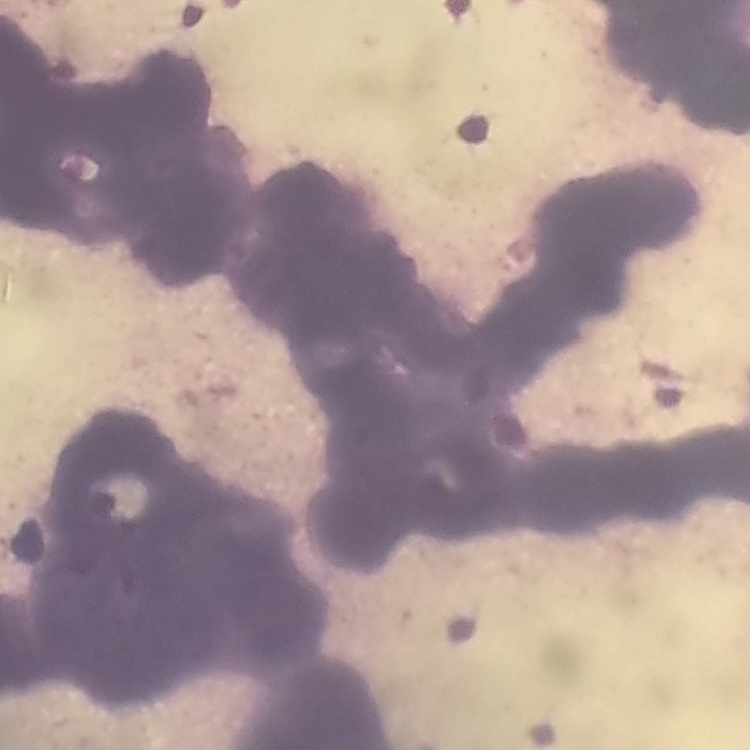

The red blood cells show rouleaux formation. Square crop of a larger photomicrograph. Field's or Giemsa stain. Thin blood smear.